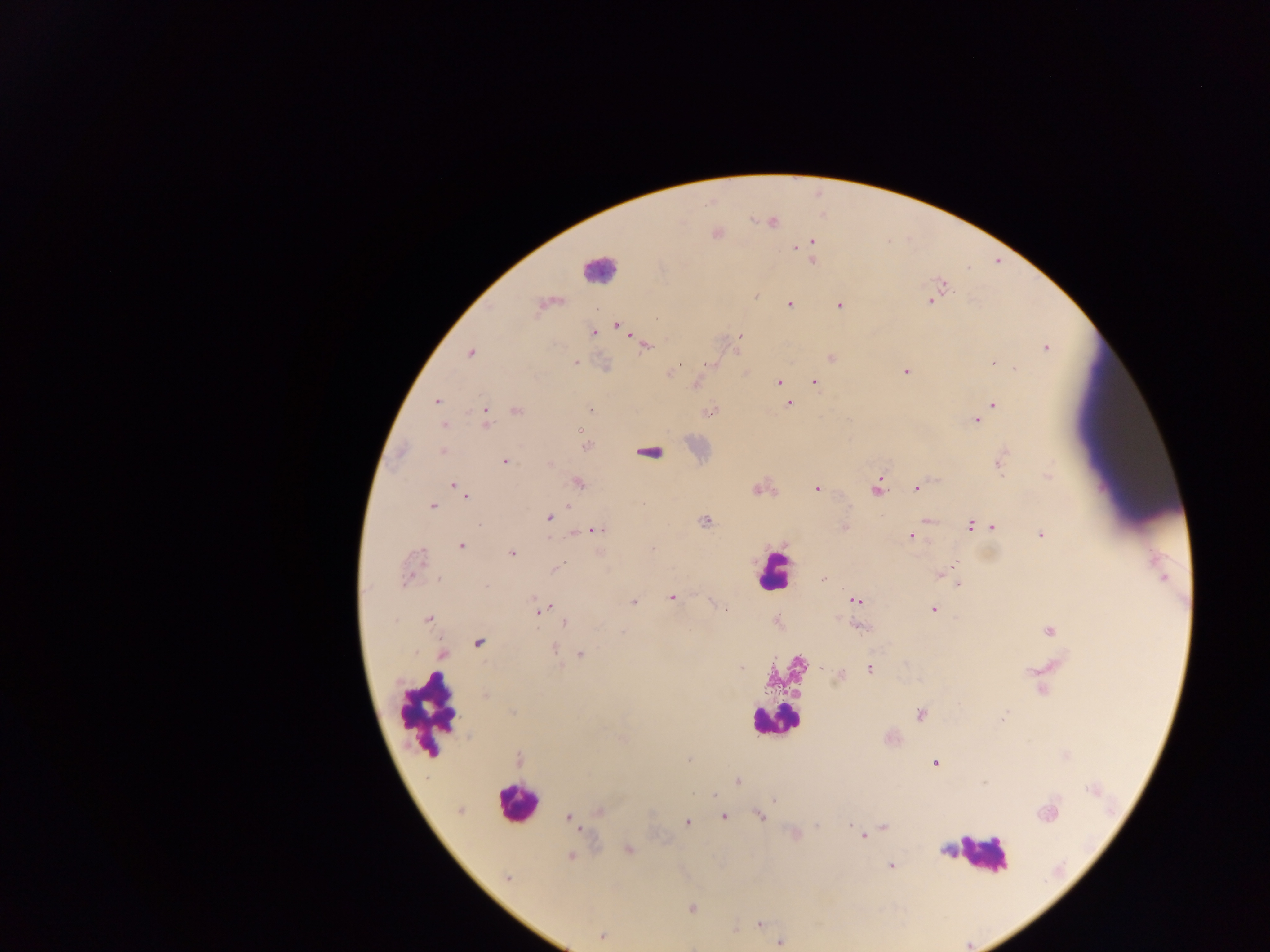

Approximate centers as {x, y} in pixels.
Summary:
  - Malaria parasite locations: {771, 222}, {716, 233}, {812, 242}, {804, 245}, {797, 247}, {813, 252}, {813, 258}, {942, 286}, {755, 295}, {935, 295}, {931, 300}, {548, 302}, {789, 304}, {838, 305}, {617, 325}, {593, 332}, {740, 336}, {645, 344}, {1045, 347}, {470, 352}, {832, 358}, {575, 361}, {992, 361}, {709, 364}, {606, 366}, {1014, 369}, {906, 371}, {669, 373}, {780, 382}, {814, 382}, {695, 384}, {784, 393}, {437, 401}, {788, 403}, {992, 404}, {591, 409}, {710, 410}, {516, 411}, {485, 417}, {977, 420}, {444, 425}, {586, 446}, {443, 451}, {504, 461}, {998, 462}, {550, 464}, {1048, 476}, {577, 482}, {455, 486}, {460, 487}, {877, 487}, {758, 488}, {915, 488}, {816, 489}, {464, 496}, {431, 505}, {548, 517}, {926, 520}, {705, 522}, {970, 524}, {992, 526}, {844, 527}, {595, 530}, {575, 532}, {1041, 535}, {910, 536}, {460, 545}, {652, 550}, {511, 553}, {411, 565}, {555, 568}, {940, 574}, {823, 579}, {957, 583}, {671, 597}, {855, 600}, {634, 601}, {539, 608}, {933, 609}, {428, 618}, {565, 622}, {856, 625}, {1049, 630}, {478, 643}, {553, 648}, {442, 654}, {581, 654}, {740, 668}, {822, 668}, {870, 668}, {840, 674}, {920, 714}, {1003, 717}, {688, 758}, {519, 759}, {935, 763}, {737, 780}, {460, 810}, {599, 811}, {1047, 813}, {759, 815}, {723, 816}, {568, 819}, {686, 822}, {883, 827}, {794, 834}, {862, 835}, {628, 849}, {947, 850}, {571, 856}, {891, 866}, {508, 878}, {692, 908}, {760, 923}, {735, 930}, {601, 936}, {779, 940}
  - Leukocyte locations: {598, 270}, {649, 451}, {774, 570}, {429, 712}, {774, 721}, {517, 802}, {982, 854}
  - Image size: 1270×952 pixels
  - Capture: mobile-phone photograph through a microscope
  - Field of view: single
  - Preparation: thick blood smear
  - Country: Ghana